Assess this cell for malaria.
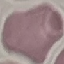

Uninfected.

{
  "capture": "smartphone through the microscope eyepiece",
  "image_type": "cell patch, automatically extracted from a larger field of view and resized to 64 × 64 pixels",
  "preparation": "thin smear",
  "stain": "Giemsa"
}